Assess the morphology of the erythrocytes.
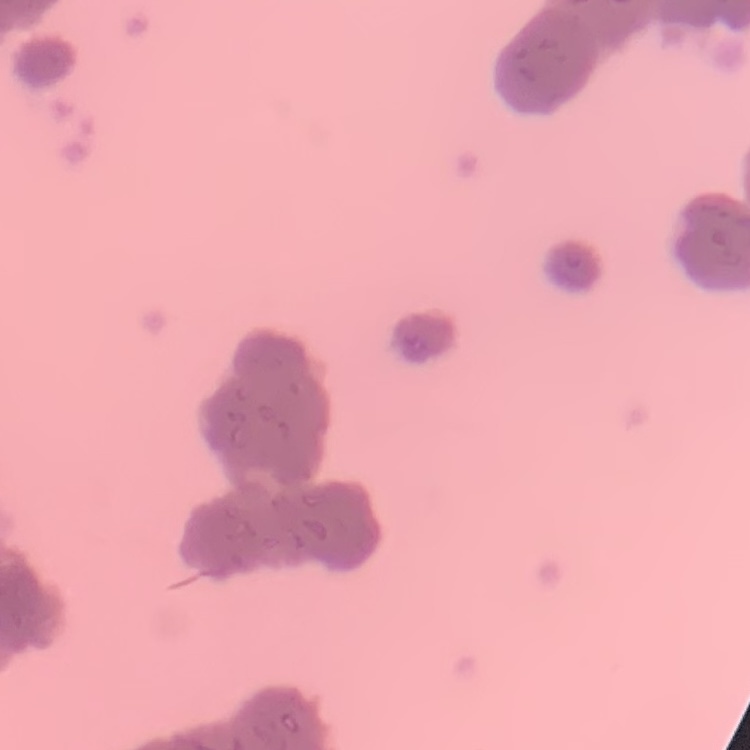
They show rouleaux formation.

{
  "image_type": "square crop of a larger photomicrograph",
  "stain": "Field's or Giemsa",
  "preparation": "thin blood smear"
}